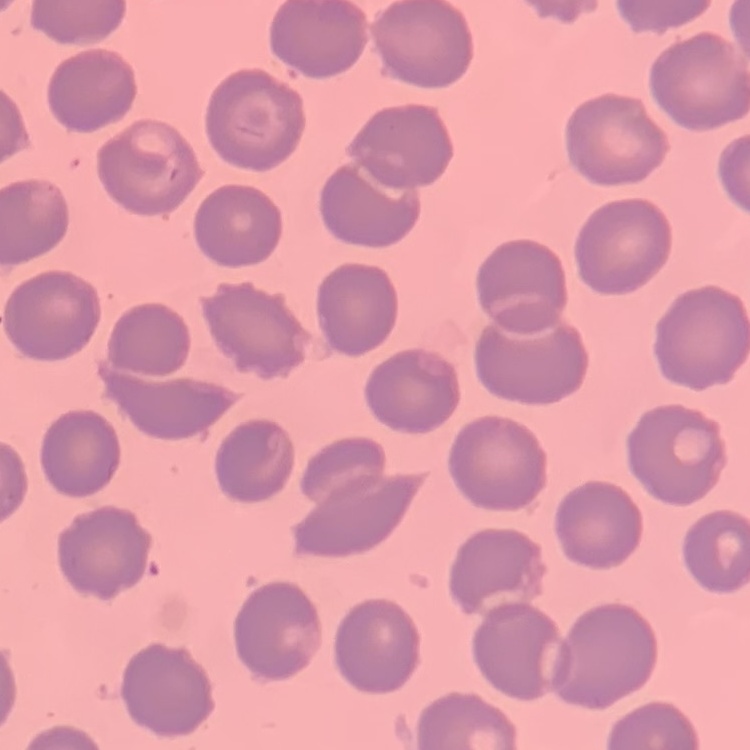
erythrocyte morphology = no rouleaux formation
preparation = thin blood smear
image type = one tile cut from a larger photomicrograph
stain = Field's or Giemsa